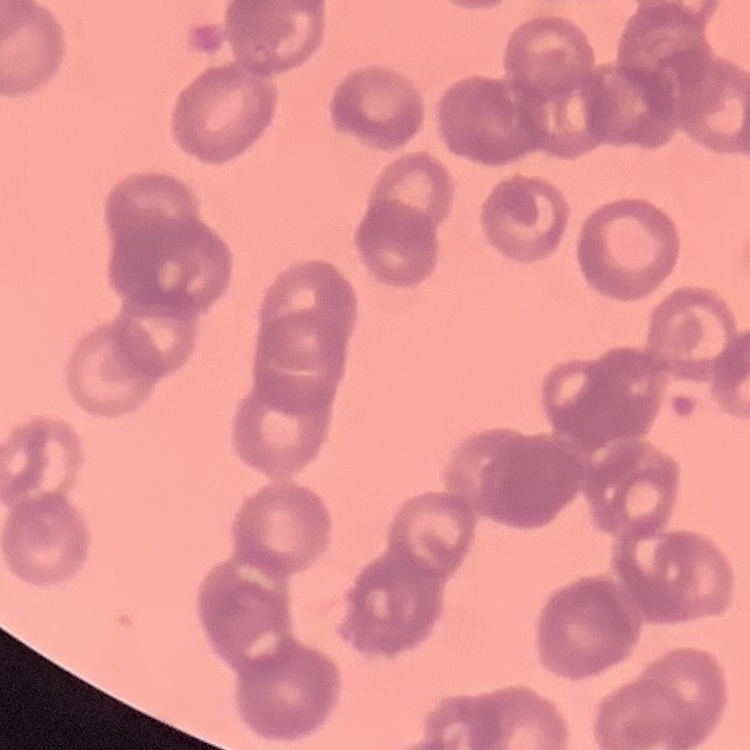

red blood cell morphology = rouleaux formation
stain = Field's or Giemsa
image type = square crop of a larger photomicrograph
preparation = thin peripheral smear